Name the blood parasite species.
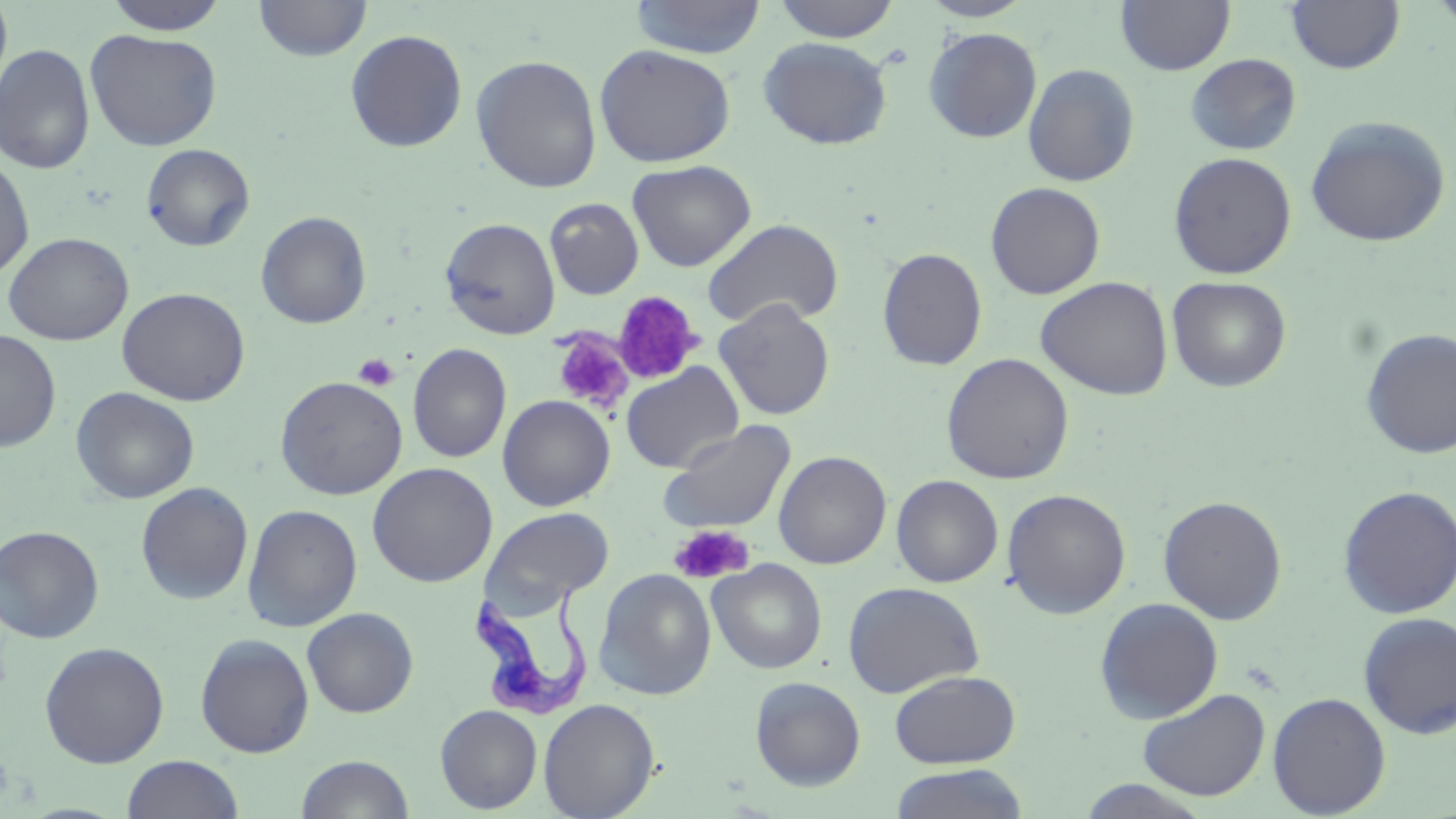

Trypanosoma brucei.

Approximate bounding boxes as [x1, y1, x2, y2] in pixels. Trypanosoma brucei locations: [467, 586, 594, 721]. Platelet locations: [611, 292, 705, 386], [552, 331, 633, 413], [353, 353, 399, 391], [669, 525, 753, 585]. Uninfected red blood cell locations: [0, 0, 13, 108], [101, 0, 231, 35], [253, 0, 372, 61], [630, 0, 766, 60], [770, 0, 902, 42], [918, 0, 1035, 22], [1115, 0, 1236, 75], [1285, 0, 1405, 73], [1429, 0, 1456, 37], [923, 27, 1042, 143], [85, 29, 223, 151], [345, 29, 468, 152], [758, 37, 893, 150], [0, 44, 95, 174], [593, 44, 736, 168], [1185, 53, 1302, 156], [471, 54, 603, 193], [1023, 63, 1140, 186], [1304, 115, 1452, 248], [140, 143, 255, 252], [0, 152, 35, 283], [1168, 152, 1297, 279], [627, 160, 756, 272], [985, 182, 1105, 299], [544, 198, 644, 300], [255, 211, 372, 329], [440, 217, 561, 340], [702, 218, 844, 329], [2, 232, 134, 346], [877, 247, 988, 370], [1036, 276, 1174, 401], [1167, 276, 1291, 392], [116, 287, 251, 406], [714, 299, 836, 420], [1360, 328, 1456, 459], [0, 331, 61, 452], [407, 343, 512, 463], [941, 353, 1074, 485], [620, 362, 744, 474], [275, 376, 408, 500], [71, 387, 199, 504], [497, 394, 615, 511], [660, 421, 796, 535], [773, 450, 891, 569], [367, 462, 498, 587], [891, 474, 1003, 588], [136, 482, 253, 604], [1337, 484, 1456, 619], [1002, 488, 1131, 619], [1157, 495, 1288, 625], [242, 503, 363, 632], [481, 507, 615, 615], [0, 525, 104, 644], [708, 559, 827, 674], [594, 568, 716, 701], [843, 581, 985, 697], [1094, 597, 1224, 723], [302, 607, 419, 717], [1357, 611, 1456, 740], [195, 633, 315, 758], [39, 641, 170, 768], [889, 669, 1020, 768], [749, 676, 866, 791], [1137, 688, 1270, 801], [1267, 692, 1391, 817], [538, 698, 660, 819], [435, 705, 542, 813], [295, 754, 414, 818], [121, 755, 244, 819], [888, 764, 1030, 819], [1077, 779, 1214, 818]. Captured at 1000x magnification. Thin blood film. Single field of view. Image is 1456×819 pixels. Light microscopy. May-Grünwald-Giemsa stain.